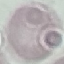

Summary:
  - Result: no malaria parasites seen
  - Image type: automatically extracted cell patch, resized to 64 × 64 pixels
  - Stain: Giemsa
  - Preparation: thin blood film
  - Capture: smartphone through the microscope eyepiece